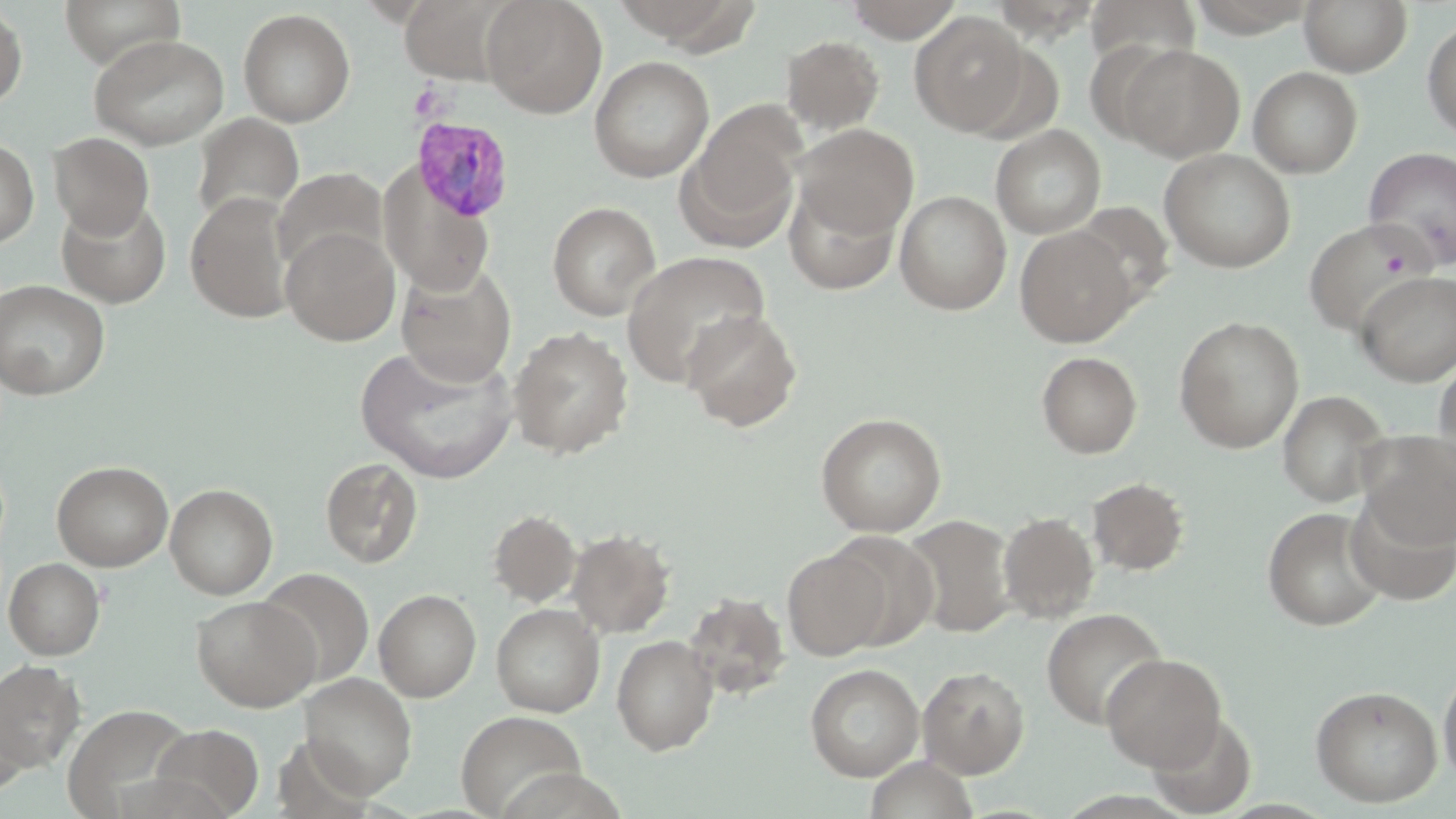

Summary:
  - Coordinate format: approximate bounding boxes as [x1, y1, x2, y2] in pixels
  - Plasmodium vivax-infected red blood cell locations: [412, 116, 517, 223]
  - Uninfected red blood cell locations: [59, 0, 185, 70], [482, 0, 607, 118], [843, 0, 966, 42], [1185, 0, 1320, 36], [1299, 0, 1412, 75], [986, 1, 1107, 41], [0, 4, 28, 110], [238, 8, 355, 127], [910, 12, 1031, 136], [1422, 16, 1456, 143], [88, 33, 230, 148], [781, 35, 884, 135], [1117, 44, 1244, 161], [590, 55, 713, 183], [1248, 67, 1363, 177], [679, 105, 805, 250], [192, 113, 304, 227], [792, 123, 918, 240], [990, 125, 1105, 239], [48, 132, 154, 238], [0, 138, 38, 248], [1363, 147, 1456, 270], [1160, 149, 1296, 272], [273, 167, 388, 273], [381, 168, 495, 296], [783, 180, 902, 295], [894, 190, 1012, 314], [185, 192, 295, 324], [56, 196, 172, 307], [547, 201, 661, 320], [1301, 218, 1436, 337], [1015, 226, 1137, 346], [281, 227, 400, 346], [621, 251, 771, 387], [395, 262, 516, 386], [1356, 271, 1456, 385], [0, 279, 111, 400], [682, 309, 802, 432], [1174, 316, 1305, 453], [508, 326, 634, 458], [356, 343, 518, 483], [1036, 351, 1143, 458], [1433, 353, 1456, 482], [1276, 390, 1392, 506], [815, 412, 947, 537], [1357, 430, 1455, 548], [320, 457, 422, 569], [51, 460, 173, 571], [1087, 477, 1189, 576], [165, 483, 278, 599], [1345, 491, 1455, 606], [1263, 507, 1387, 631], [488, 509, 581, 607], [997, 512, 1099, 623], [903, 514, 1015, 637], [567, 528, 675, 637], [827, 530, 939, 650], [782, 547, 890, 660], [3, 557, 105, 660], [255, 567, 374, 687], [374, 589, 481, 702], [684, 592, 790, 700], [191, 595, 320, 711], [491, 604, 604, 716], [1041, 607, 1167, 729], [611, 634, 718, 754], [1100, 653, 1226, 771], [0, 660, 84, 771], [1438, 662, 1456, 786], [805, 663, 924, 781], [918, 666, 1029, 778], [299, 674, 417, 797], [1310, 684, 1443, 807], [0, 691, 31, 797], [64, 703, 195, 817], [455, 710, 586, 818], [1145, 711, 1258, 817], [150, 724, 263, 818], [864, 755, 979, 819]
  - Slide-level diagnosis: Plasmodium vivax
  - Modality: optical microscopy
  - Preparation: thin blood film
  - Image size: 1456×819 pixels
  - Magnification: 1000x
  - Stain: May-Grünwald-Giemsa
  - Field of view: single